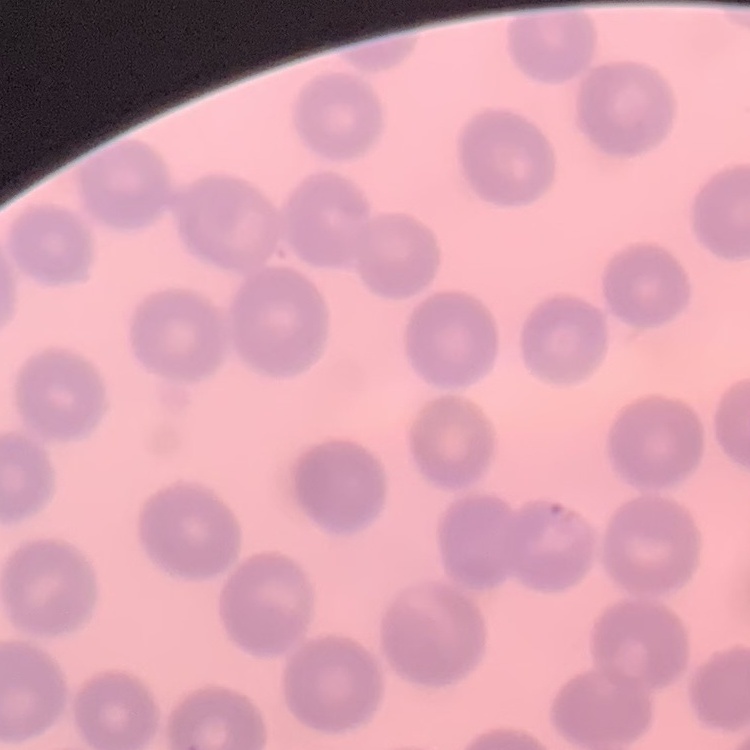

erythrocyte_morphology: no rouleaux formation
preparation: thin peripheral smear
image_type: one tile cut from a larger photomicrograph
stain: Field's or Giemsa